Describe the morphology of the red blood cells.
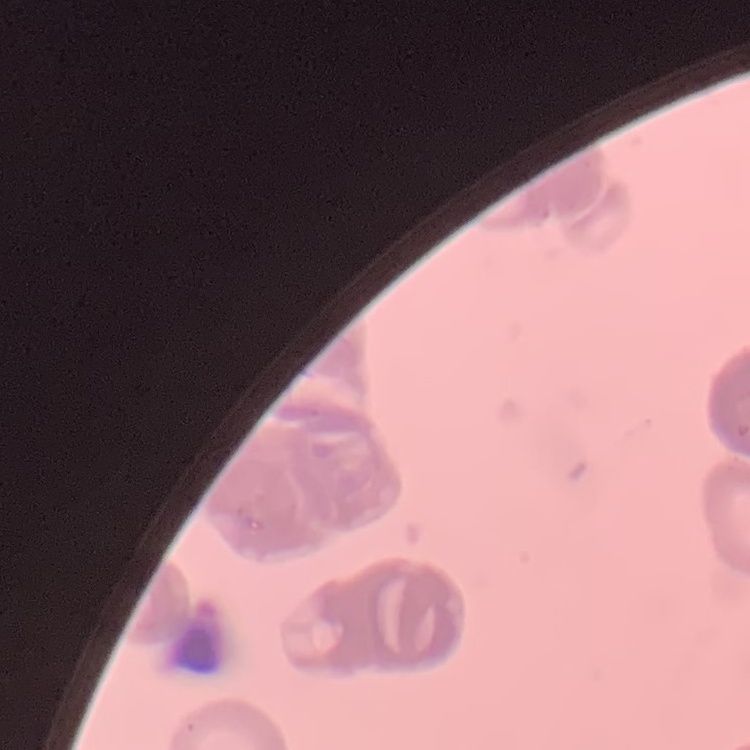

Rouleaux formation.

Stained with either Field's or Giemsa. Square crop of a larger photomicrograph. Thin blood smear.